Name the cell type shown.
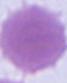
An erythrocyte.

modality = micrograph
magnification = 1000x